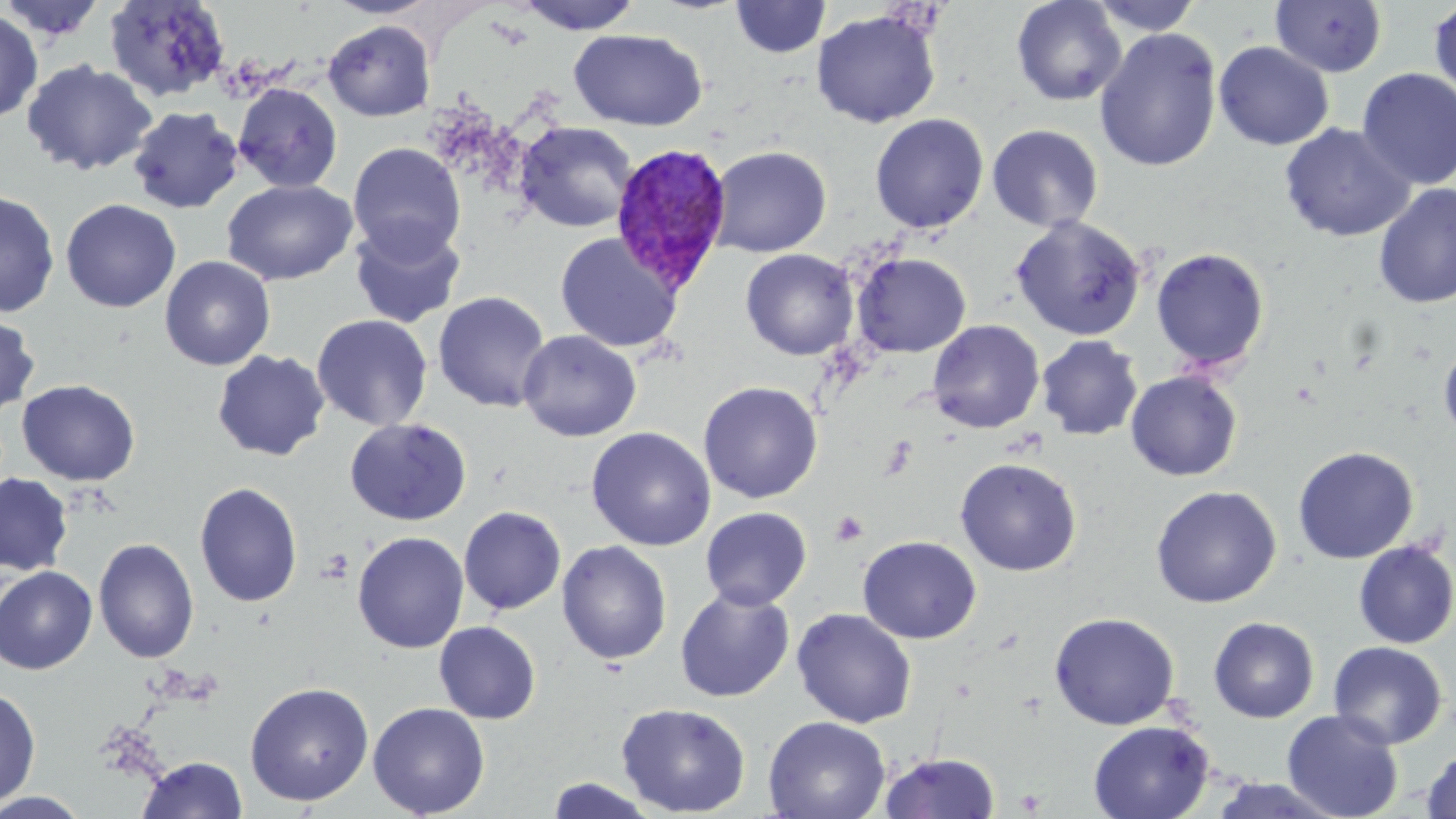
slide-level diagnosis = Plasmodium vivax
uninfected red blood cell locations = approximate bounding boxes as [x1, y1, x2, y2] in pixels: [1, 0, 107, 44], [104, 0, 230, 101], [513, 0, 644, 34], [730, 0, 831, 59], [1010, 0, 1127, 106], [1089, 0, 1204, 36], [1429, 0, 1456, 104], [1270, 1, 1388, 77], [0, 9, 43, 124], [810, 10, 941, 128], [323, 19, 435, 121], [569, 28, 707, 131], [1094, 28, 1222, 171], [1213, 41, 1334, 151], [22, 59, 157, 176], [1355, 68, 1456, 190], [233, 83, 343, 193], [128, 106, 243, 214], [869, 113, 989, 233], [515, 121, 637, 232], [1279, 123, 1416, 243], [986, 124, 1103, 233], [348, 143, 466, 262], [708, 145, 832, 257], [221, 179, 357, 286], [1373, 184, 1456, 308], [0, 190, 60, 318], [60, 199, 181, 312], [1010, 215, 1147, 341], [349, 221, 466, 330], [555, 232, 684, 353], [1150, 247, 1270, 374], [740, 248, 859, 360], [852, 252, 972, 358], [159, 255, 276, 371], [433, 291, 552, 413], [0, 312, 40, 418], [311, 314, 433, 431], [927, 319, 1045, 434], [518, 330, 641, 442], [1036, 335, 1143, 440], [1439, 341, 1456, 445], [212, 349, 330, 461], [1125, 370, 1243, 481], [16, 379, 141, 486], [698, 381, 823, 504], [344, 417, 472, 526], [586, 426, 716, 551], [1292, 445, 1419, 564], [955, 457, 1082, 576], [0, 473, 73, 575], [194, 482, 303, 607], [1149, 485, 1282, 608], [459, 506, 566, 614], [700, 507, 812, 610], [352, 531, 469, 653], [857, 535, 981, 643], [93, 538, 199, 664], [556, 540, 672, 664], [1353, 540, 1456, 649], [0, 566, 98, 674], [675, 587, 795, 702], [791, 608, 916, 728], [1048, 612, 1179, 730], [1208, 616, 1319, 723], [434, 621, 541, 724], [1328, 641, 1448, 749], [244, 681, 374, 806], [0, 686, 41, 808], [367, 702, 491, 817], [616, 702, 751, 817], [1282, 709, 1404, 819], [763, 715, 890, 819], [1088, 720, 1215, 819], [1420, 749, 1456, 818], [879, 751, 1001, 819], [138, 756, 249, 818], [546, 777, 659, 818], [1206, 777, 1348, 818], [0, 791, 92, 818]
platelet locations = approximate bounding boxes as [x1, y1, x2, y2] in pixels: [830, 510, 869, 547], [316, 551, 353, 584]
modality = light microscopy
field of view = one of a larger specimen
stain = May-Grünwald-Giemsa
image size = 1456×819 pixels
magnification = 1000x
preparation = thin blood film
Plasmodium vivax-infected red blood cell locations = approximate bounding boxes as [x1, y1, x2, y2] in pixels: [609, 141, 733, 294]